Locate every uninfected red blood cell.
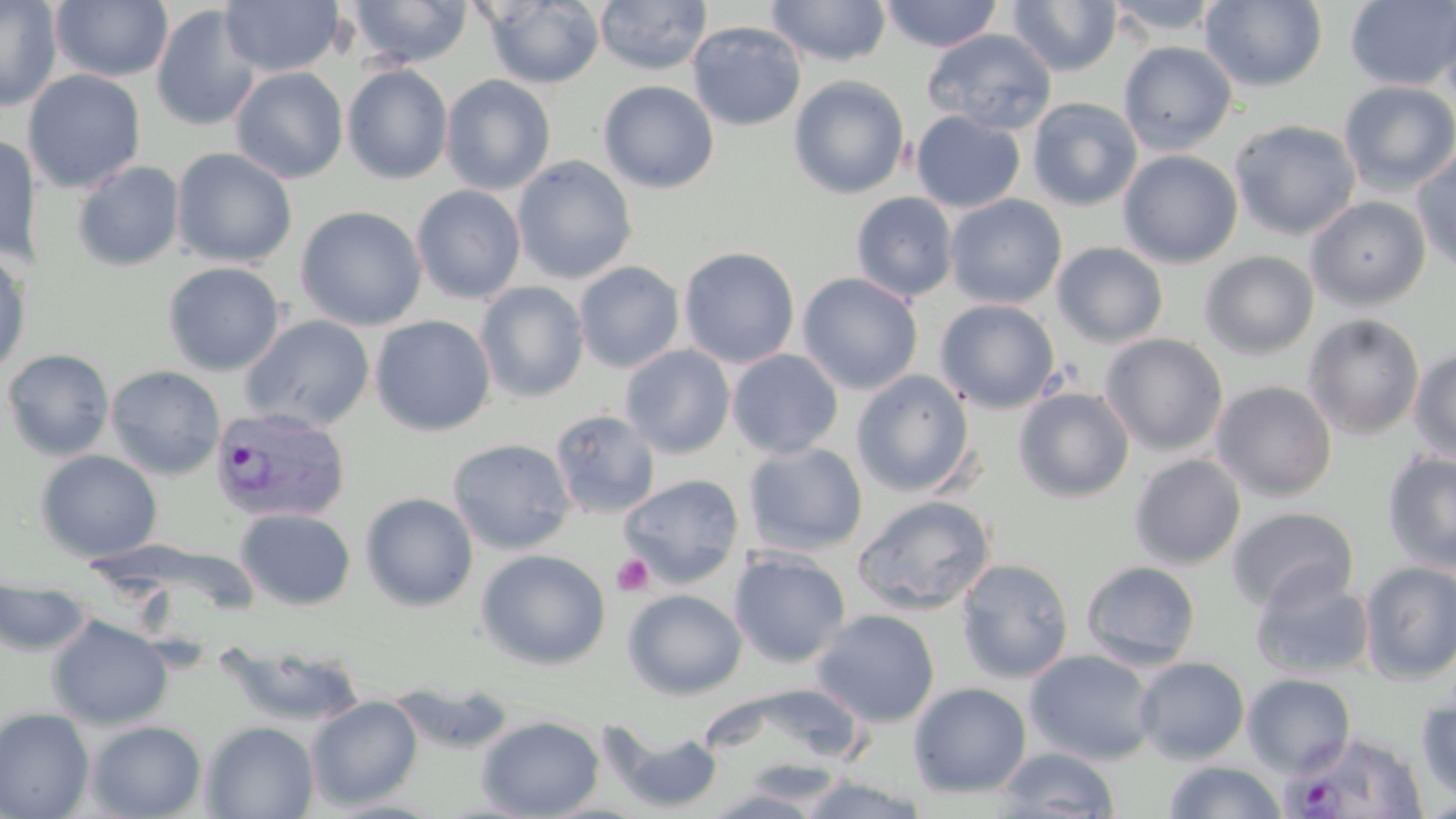
Approximate bounding boxes as named x1/y1/x2/y2 corners in pixels.
Uninfected red blood cells: (x1=0, y1=0, x2=62, y2=112), (x1=50, y1=0, x2=174, y2=82), (x1=220, y1=0, x2=343, y2=77), (x1=349, y1=0, x2=472, y2=68), (x1=594, y1=0, x2=712, y2=75), (x1=766, y1=0, x2=892, y2=67), (x1=879, y1=0, x2=1004, y2=52), (x1=1007, y1=0, x2=1122, y2=76), (x1=1104, y1=0, x2=1224, y2=37), (x1=1200, y1=0, x2=1327, y2=91), (x1=1345, y1=0, x2=1456, y2=91), (x1=1436, y1=0, x2=1456, y2=116), (x1=481, y1=1, x2=604, y2=88), (x1=150, y1=3, x2=262, y2=132), (x1=687, y1=21, x2=807, y2=131), (x1=922, y1=28, x2=1057, y2=135), (x1=1119, y1=41, x2=1237, y2=155), (x1=342, y1=64, x2=453, y2=184), (x1=230, y1=66, x2=348, y2=183), (x1=958, y1=68, x2=1112, y2=215), (x1=23, y1=70, x2=146, y2=193), (x1=441, y1=74, x2=556, y2=195), (x1=788, y1=75, x2=910, y2=199), (x1=598, y1=80, x2=719, y2=193), (x1=1338, y1=81, x2=1456, y2=196), (x1=1027, y1=97, x2=1143, y2=211), (x1=911, y1=111, x2=1025, y2=213), (x1=1229, y1=120, x2=1361, y2=241), (x1=0, y1=132, x2=39, y2=265), (x1=171, y1=147, x2=297, y2=268), (x1=1412, y1=147, x2=1456, y2=273), (x1=1118, y1=150, x2=1243, y2=268), (x1=512, y1=156, x2=637, y2=284), (x1=72, y1=161, x2=185, y2=271), (x1=411, y1=185, x2=526, y2=303), (x1=851, y1=192, x2=959, y2=302), (x1=944, y1=194, x2=1067, y2=309), (x1=1306, y1=196, x2=1430, y2=310), (x1=295, y1=205, x2=428, y2=331), (x1=1052, y1=242, x2=1169, y2=348), (x1=678, y1=246, x2=800, y2=367), (x1=0, y1=251, x2=30, y2=377), (x1=1199, y1=251, x2=1320, y2=359), (x1=162, y1=261, x2=284, y2=376), (x1=574, y1=261, x2=685, y2=373), (x1=796, y1=272, x2=923, y2=395), (x1=475, y1=281, x2=590, y2=403), (x1=935, y1=298, x2=1061, y2=413), (x1=1303, y1=314, x2=1425, y2=439), (x1=240, y1=315, x2=375, y2=432), (x1=369, y1=315, x2=496, y2=436), (x1=1100, y1=333, x2=1228, y2=456), (x1=620, y1=345, x2=735, y2=458), (x1=1408, y1=347, x2=1456, y2=464), (x1=1, y1=348, x2=115, y2=462), (x1=727, y1=349, x2=843, y2=459), (x1=106, y1=365, x2=225, y2=480), (x1=851, y1=370, x2=976, y2=497), (x1=1211, y1=380, x2=1337, y2=501), (x1=1013, y1=388, x2=1134, y2=503), (x1=550, y1=409, x2=661, y2=518), (x1=448, y1=439, x2=575, y2=555), (x1=743, y1=443, x2=868, y2=556), (x1=36, y1=450, x2=162, y2=563), (x1=1382, y1=452, x2=1456, y2=574), (x1=1129, y1=454, x2=1246, y2=569), (x1=618, y1=474, x2=745, y2=588), (x1=360, y1=492, x2=479, y2=612), (x1=853, y1=495, x2=996, y2=615), (x1=1228, y1=507, x2=1359, y2=614), (x1=235, y1=508, x2=356, y2=610), (x1=476, y1=549, x2=612, y2=670), (x1=729, y1=549, x2=851, y2=668), (x1=956, y1=558, x2=1074, y2=683), (x1=1080, y1=560, x2=1202, y2=670), (x1=1359, y1=560, x2=1456, y2=683), (x1=1251, y1=573, x2=1375, y2=680), (x1=0, y1=580, x2=91, y2=656), (x1=622, y1=589, x2=747, y2=700), (x1=811, y1=609, x2=940, y2=727), (x1=46, y1=615, x2=173, y2=730), (x1=215, y1=640, x2=368, y2=729), (x1=1025, y1=650, x2=1159, y2=765), (x1=1134, y1=656, x2=1250, y2=764), (x1=1241, y1=673, x2=1356, y2=777), (x1=387, y1=681, x2=517, y2=755), (x1=908, y1=682, x2=1032, y2=798), (x1=1416, y1=690, x2=1456, y2=807), (x1=306, y1=696, x2=424, y2=810), (x1=0, y1=707, x2=95, y2=819), (x1=476, y1=714, x2=605, y2=818), (x1=85, y1=720, x2=207, y2=818), (x1=201, y1=720, x2=319, y2=818), (x1=604, y1=722, x2=723, y2=814), (x1=995, y1=747, x2=1121, y2=818), (x1=1162, y1=760, x2=1288, y2=819), (x1=795, y1=774, x2=931, y2=817), (x1=702, y1=787, x2=833, y2=818).

slide-level diagnosis = Plasmodium vivax
preparation = thin blood smear
image size = 1456×819 pixels
magnification = 1000x
field of view = one of a larger specimen
Plasmodium vivax-infected red blood cell locations = approximate bounding boxes as named x1/y1/x2/y2 corners in pixels: (x1=209, y1=406, x2=350, y2=524), (x1=1284, y1=730, x2=1429, y2=818)
platelet locations = approximate bounding boxes as named x1/y1/x2/y2 corners in pixels: (x1=611, y1=554, x2=654, y2=596)
modality = optical microscopy
stain = May-Grünwald-Giemsa